Identify the cell.
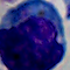
A leukocyte.

Summary:
  - Magnification: 1000x
  - Modality: photomicrograph